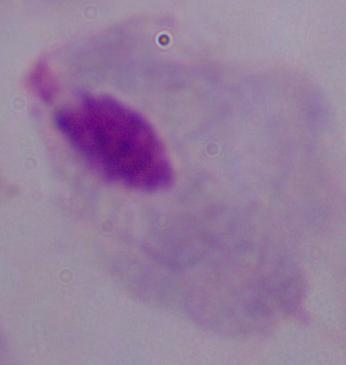
Captured at 1000x magnification. Photomicrograph. A trichomonad is seen.